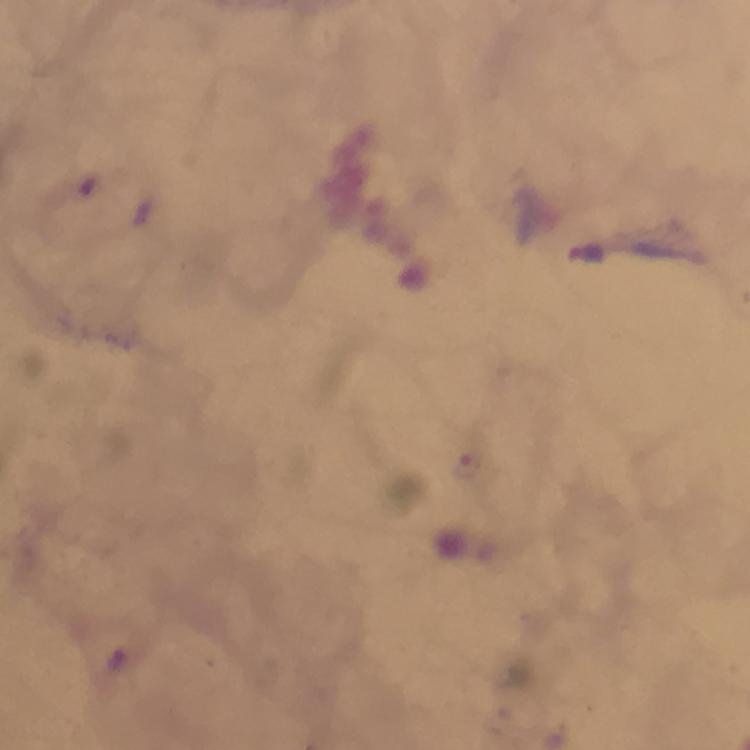

Approximate centers as (x, y) in pixels.
Summary:
  - Plasmodium parasite locations: (469, 465), (119, 661)
  - Cropped from: a single field of view
  - Capture: smartphone mounted on the microscope
  - Immersion oil: used
  - Stain: Giemsa
  - Context: from a malaria diagnostic workup
  - Preparation: thick blood film
  - Magnification: 100x
  - Image size: 750×750 pixels